Identify the preparation type.
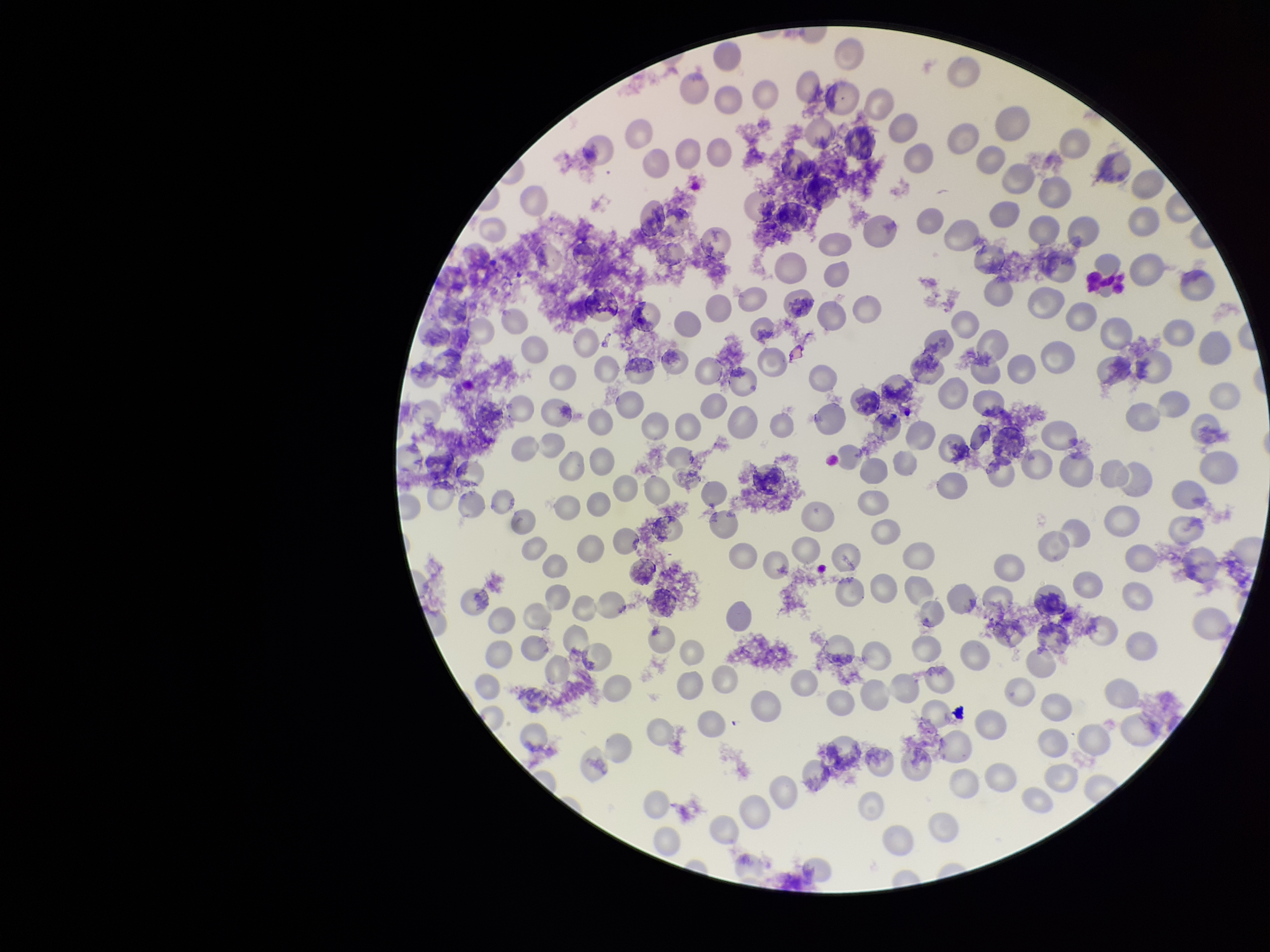
It is a thin blood smear.

parasitized red blood cell count = 0
capture = smartphone photograph through the microscope eyepiece
parasitized red blood cells = none seen
red blood cell count = 201
image size = 1270×952 pixels
species reported for this patient = Plasmodium vivax
stain = Giemsa
field of view = single
patient malaria status = positive